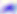

magnification = 400x
modality = micrograph
identification = Toxoplasma gondii